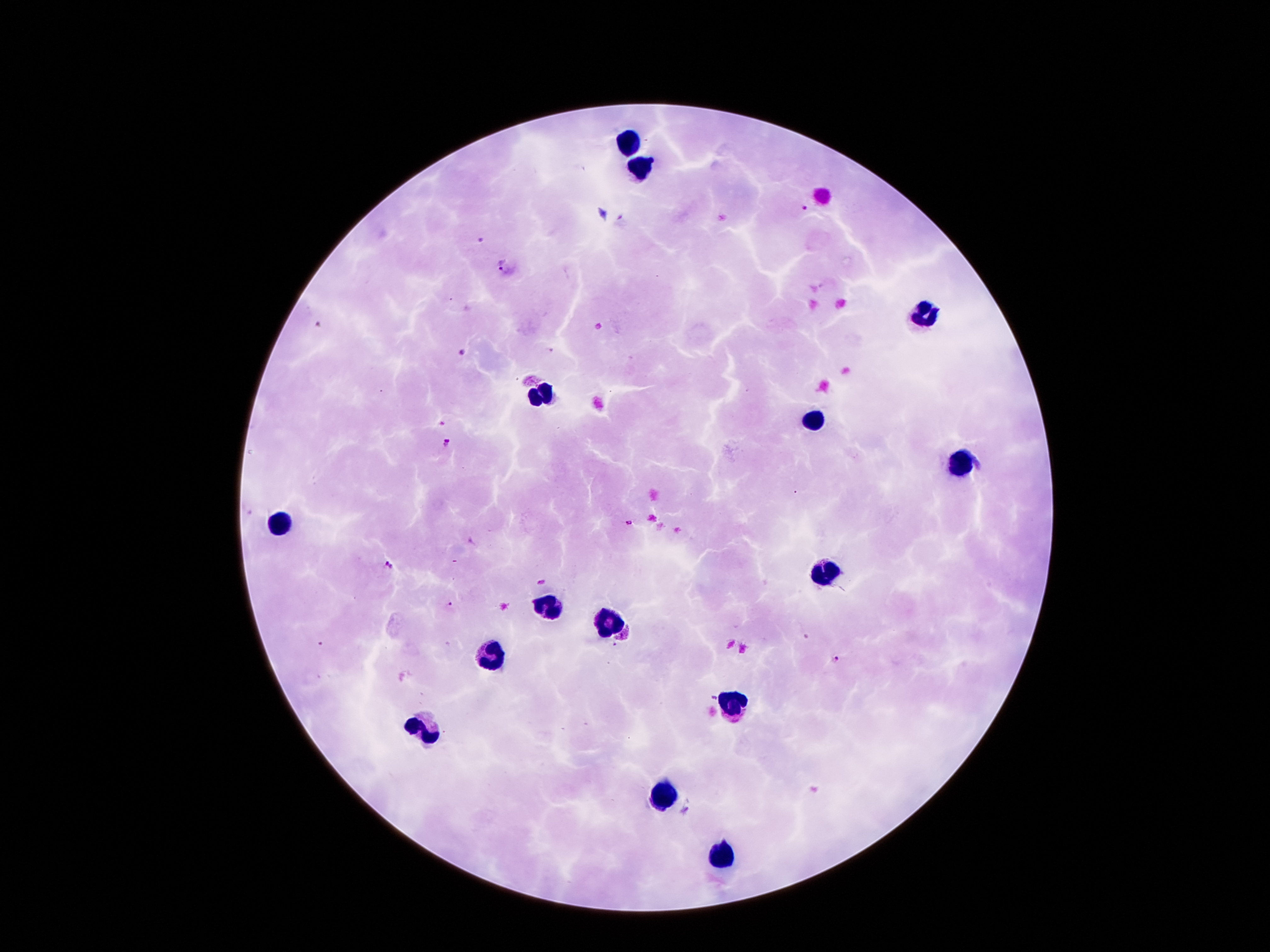
coordinate format = approximate centers as [x, y] in pixels
leukocyte locations = [627, 140], [640, 167], [923, 314], [541, 394], [812, 421], [961, 463], [279, 524], [823, 574], [545, 610], [608, 625], [493, 654], [734, 704], [426, 725], [663, 795], [720, 858]
malaria parasite locations = [804, 209], [480, 240], [503, 264], [318, 325], [461, 353], [447, 442], [630, 523], [388, 566], [450, 605], [321, 644], [836, 660], [711, 698]
stain = Giemsa
image size = 1270×952 pixels
patient malaria status = infected with Plasmodium falciparum
magnification = 100x
capture = smartphone camera through the microscope eyepiece
preparation = thick blood film
field of view = one from this slide